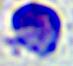
Summary:
  - Identification: leukocyte
  - Modality: photomicrograph
  - Magnification: 400x